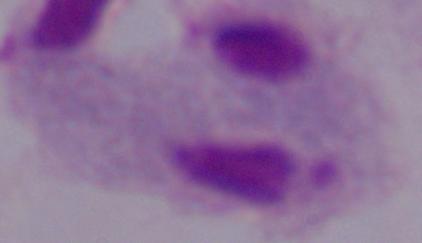

A trichomonad is shown. Micrograph. 1000x magnification.